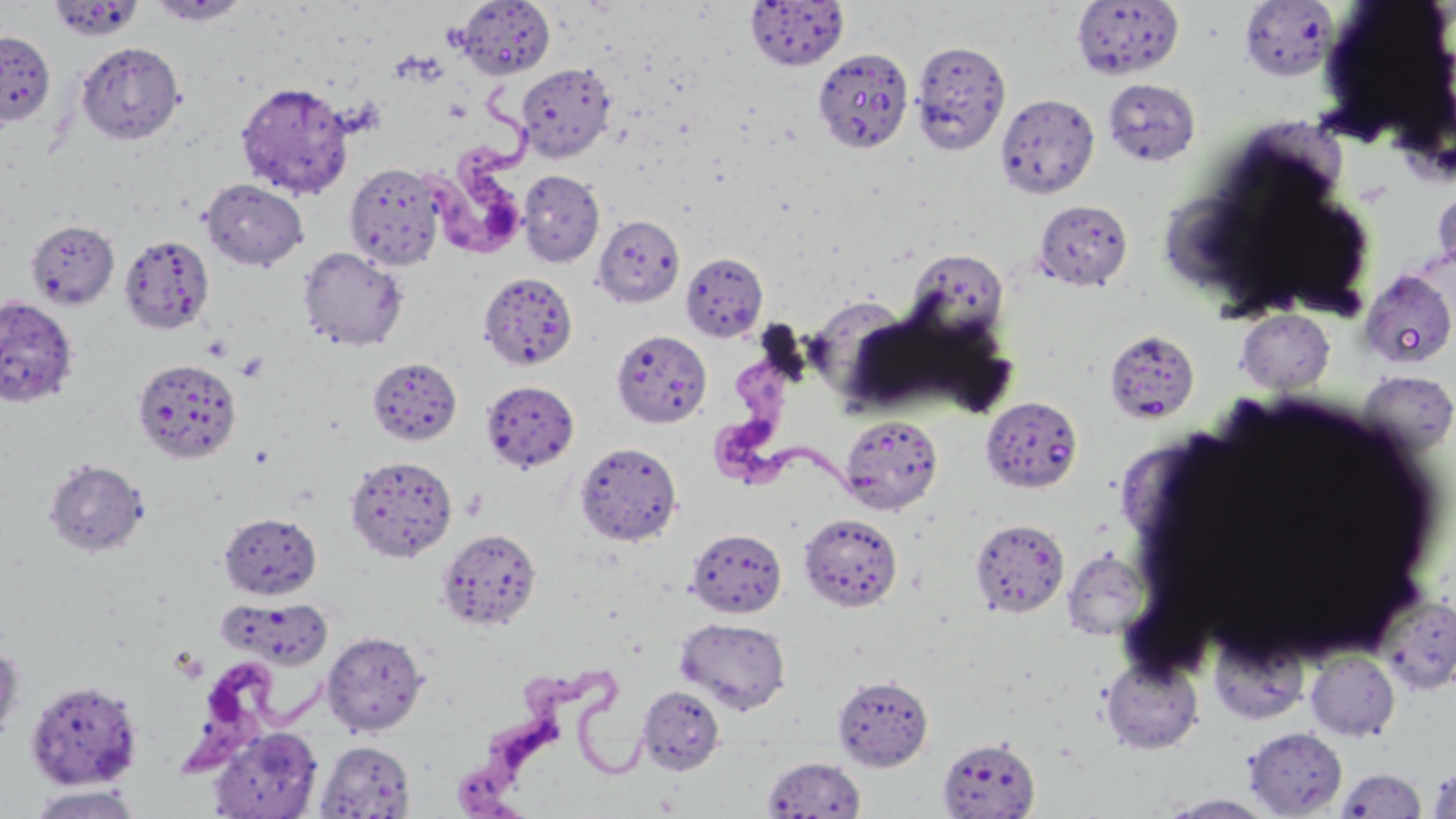

{
  "slide_level_diagnosis": "Trypanosoma brucei",
  "platelet_locations": "approximate bounding boxes as (x1,y1)-(x2,y2) corner pairs in pixels: (202,334)-(234,361), (236,352)-(269,382)",
  "stain": "May-Grünwald-Giemsa",
  "trypanosoma_brucei_locations": "approximate bounding boxes as (x1,y1)-(x2,y2) corner pairs in pixels: (421,69)-(534,263), (708,340)-(867,507), (185,656)-(328,774), (452,664)-(654,818)",
  "modality": "light microscopy",
  "magnification": "1000x",
  "preparation": "thin blood smear",
  "image_size": "1456×819 pixels",
  "uninfected_red_blood_cell_locations": "approximate bounding boxes as (x1,y1)-(x2,y2) corner pairs in pixels: (146,0)-(251,26), (456,0)-(555,77), (744,0)-(850,70), (48,1)-(145,42), (1071,1)-(1185,80), (1239,1)-(1338,82), (0,30)-(56,126), (911,39)-(1011,155), (76,41)-(185,145), (812,48)-(914,153), (515,62)-(616,162), (1102,78)-(1201,166), (236,81)-(354,199), (995,93)-(1099,199), (345,162)-(446,270), (518,170)-(605,267), (200,178)-(309,271), (1431,179)-(1456,282), (1032,199)-(1133,291), (593,214)-(685,308), (26,219)-(119,309), (119,233)-(215,335), (298,246)-(408,351), (905,249)-(1010,343), (680,252)-(769,342), (1359,270)-(1456,369), (481,272)-(581,371), (0,297)-(78,407), (1235,309)-(1335,394), (610,329)-(712,429), (1109,335)-(1199,421), (367,357)-(462,446), (133,358)-(241,463), (1356,369)-(1456,456), (480,380)-(579,473), (981,396)-(1084,493), (840,415)-(943,514), (574,441)-(682,546), (345,455)-(457,563), (44,458)-(149,557), (219,512)-(322,600), (798,512)-(904,612), (970,518)-(1070,617), (437,527)-(543,631), (686,528)-(787,618), (1063,550)-(1150,640), (1378,595)-(1456,694), (224,596)-(335,670), (675,617)-(792,714), (322,631)-(428,736), (1209,631)-(1308,725), (0,642)-(24,745), (1306,651)-(1399,741), (1101,656)-(1203,754), (833,675)-(934,771), (25,678)-(143,790), (637,685)-(725,775), (209,726)-(323,818), (1243,727)-(1348,816), (937,737)-(1040,818), (315,740)-(416,818), (762,756)-(867,818), (1427,762)-(1456,818), (1336,767)-(1428,817), (26,784)-(143,819), (1158,794)-(1278,818)",
  "field_of_view": "one of a larger specimen"
}